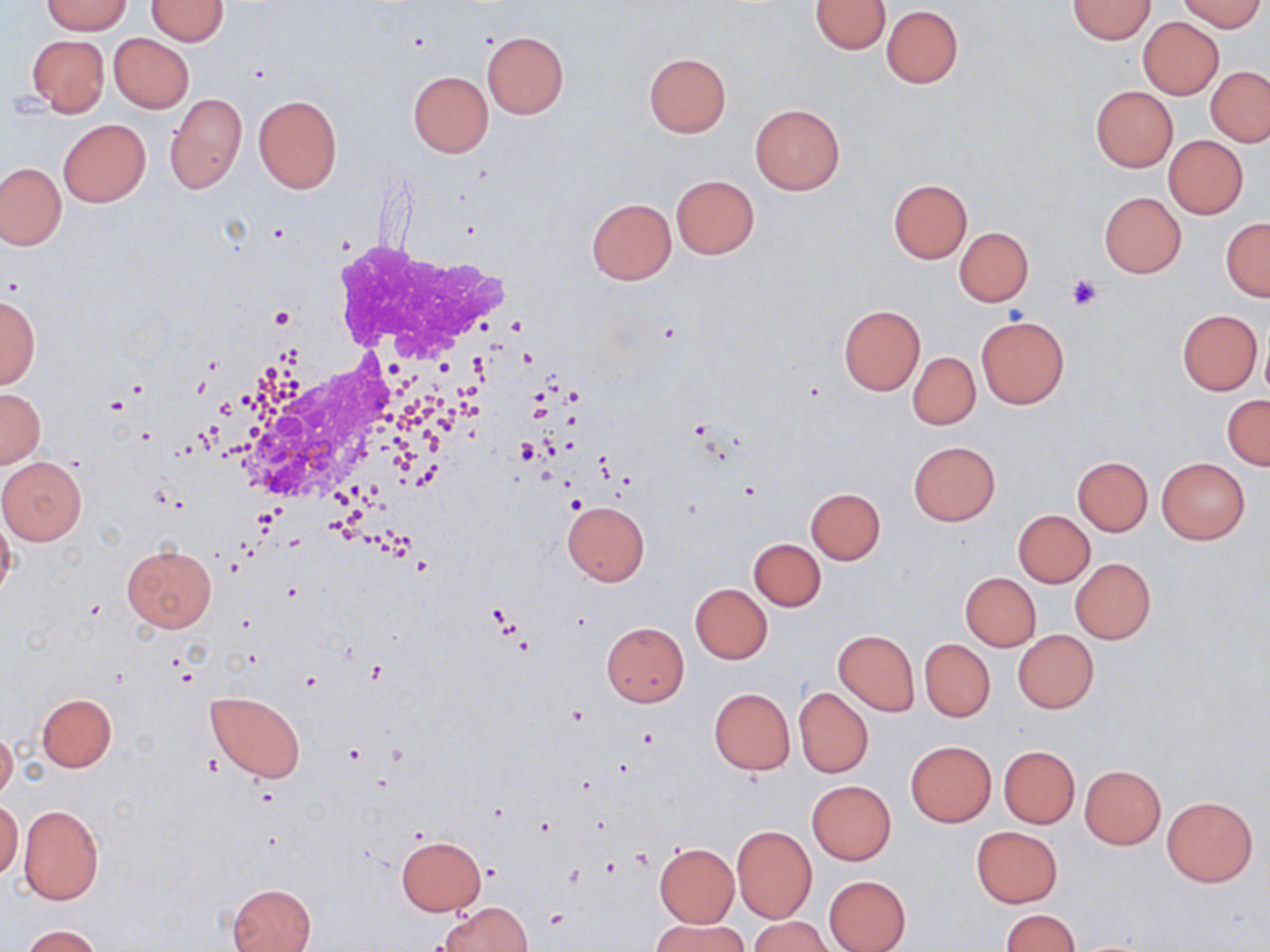

Approximate bounding boxes as (x1,y1)-(x2,y2) corner pairs in pixels. Platelet locations: (1065,274)-(1103,312). Uninfected red blood cell locations: (41,0)-(131,33), (811,0)-(891,54), (1069,0)-(1155,42), (1180,0)-(1263,32), (146,1)-(228,45), (882,6)-(963,88), (1138,17)-(1224,98), (482,32)-(569,118), (109,33)-(193,112), (27,35)-(109,116), (644,53)-(731,136), (1206,67)-(1269,146), (408,71)-(492,157), (1090,86)-(1178,172), (165,93)-(246,195), (254,96)-(342,193), (750,104)-(845,195), (59,119)-(150,206), (1164,136)-(1248,218), (0,162)-(65,250), (671,175)-(760,259), (889,180)-(971,262), (1099,192)-(1186,277), (587,199)-(676,285), (1221,218)-(1270,301), (955,227)-(1034,306), (0,295)-(40,388), (838,305)-(926,396), (1177,309)-(1262,395), (976,314)-(1069,408), (909,352)-(981,430), (0,388)-(45,469), (1223,396)-(1270,470), (909,440)-(1000,526), (0,456)-(86,544), (1073,457)-(1152,535), (1157,459)-(1249,544), (806,488)-(885,564), (562,500)-(649,586), (0,508)-(16,605), (1012,510)-(1095,587), (750,538)-(825,610), (122,545)-(217,632), (1071,559)-(1155,643), (960,572)-(1041,651), (691,584)-(772,663), (601,623)-(689,706), (833,629)-(919,714), (1013,630)-(1098,712), (921,640)-(994,722), (794,687)-(873,777), (709,688)-(795,773), (206,691)-(305,782), (37,694)-(116,771), (0,729)-(16,803), (906,741)-(996,827), (998,746)-(1079,828), (1080,765)-(1166,849), (806,780)-(897,865), (1162,796)-(1257,886), (0,799)-(23,879), (17,805)-(105,903), (732,826)-(816,923), (971,826)-(1062,907), (396,835)-(485,915), (654,843)-(739,927), (823,874)-(911,952), (228,883)-(317,952), (435,901)-(532,952), (1002,909)-(1079,952), (752,917)-(833,952), (651,918)-(748,952), (21,925)-(104,951). White blood cell locations: (199,217)-(533,538). Slide-level diagnosis: negative for blood parasites. Single field of view. Image is 1270×952 pixels. May-Grünwald-Giemsa stain. Captured at 1000x magnification. Light microscopy. Thin blood film.